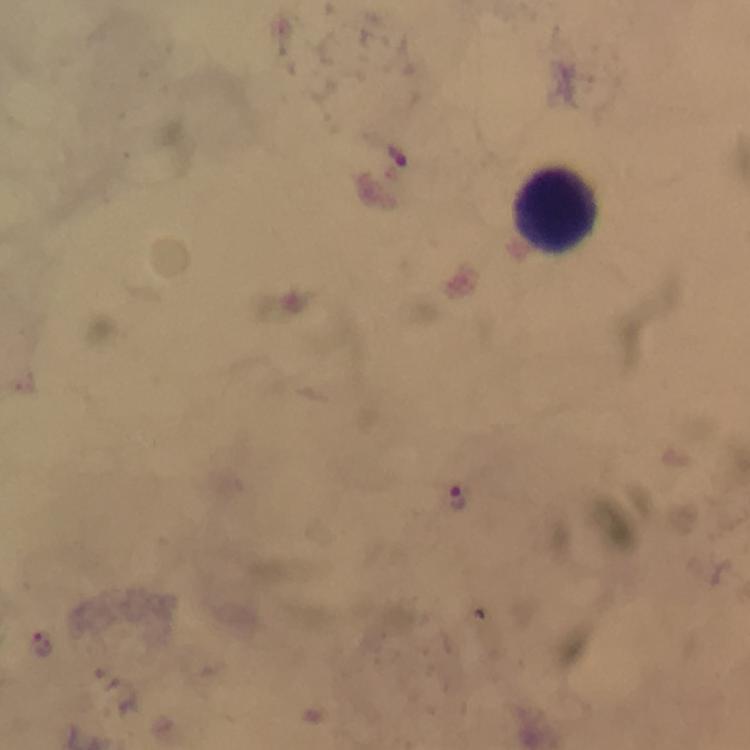

Approximate centers as {x, y} in pixels.
Summary:
  - Leukocyte locations: {558, 210}
  - Malaria parasite locations: {398, 153}, {458, 497}
  - Image size: 750×750 pixels
  - Capture: smartphone mounted on the microscope
  - Preparation: thick smear
  - Cropped from: a single field of view
  - Stain: Giemsa
  - Context: from a diagnostic examination for malaria
  - Immersion oil: applied
  - Magnification: 100x